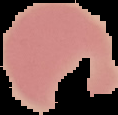

Malaria status: uninfected. From a thin blood smear. The area outside the segmented cell region is set to black. Image is 118×115 pixels.